Classify this cell by malaria status.
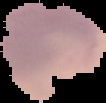
Parasitized.

From a thin blood film. Image is 106×103 pixels. The area outside the segmented cell region is set to black.